Mark where platelets are.
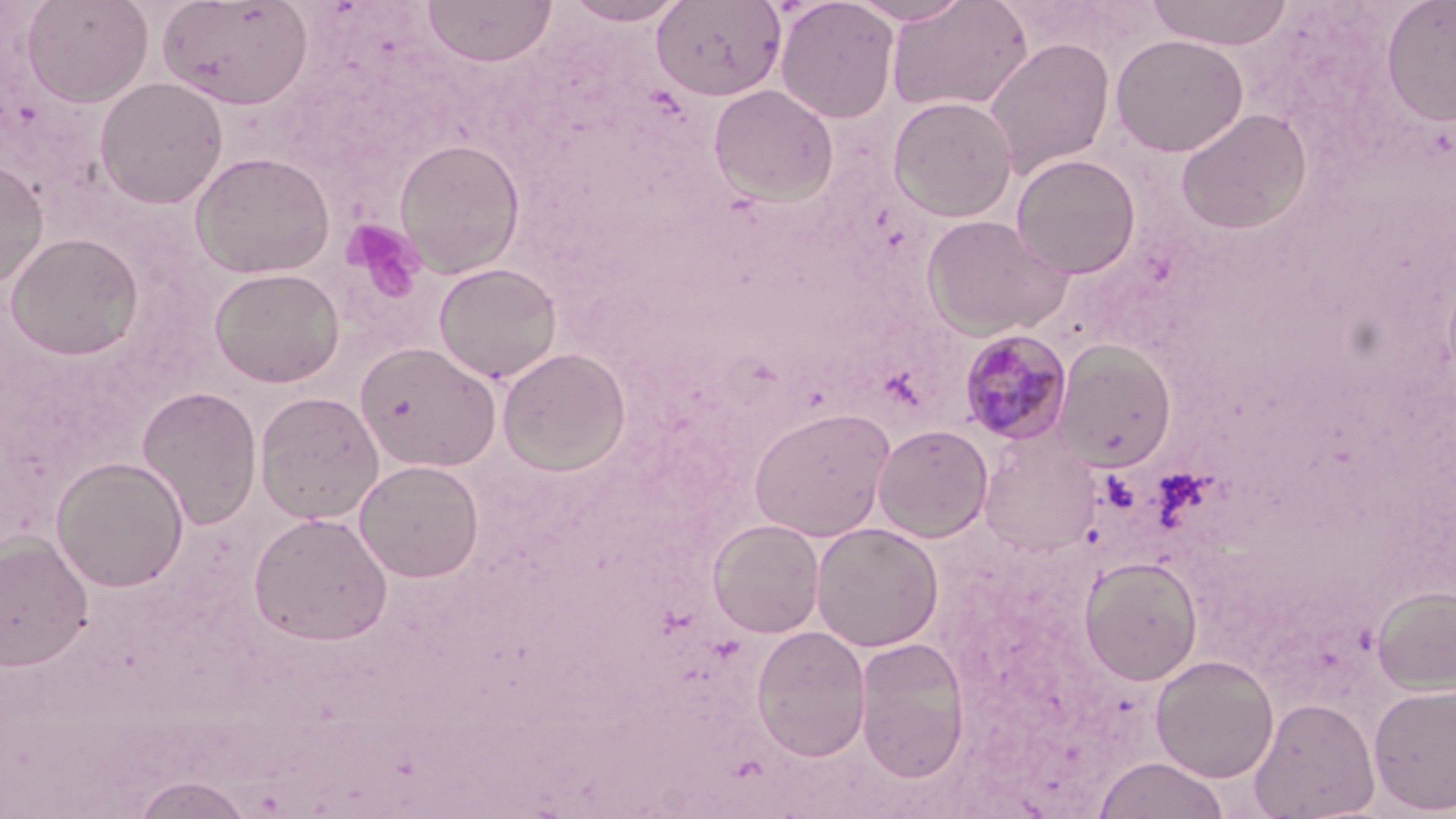
Approximate bounding boxes as (x1, y1, x2, y2) in pixels.
Platelets: (342, 218, 427, 306).

Plasmodium malariae-infected red blood cell locations: (958, 329, 1074, 445). Uninfected red blood cell locations: (22, 0, 153, 108), (422, 0, 557, 67), (651, 0, 787, 101), (775, 0, 899, 123), (847, 0, 974, 25), (886, 0, 1032, 114), (1143, 0, 1295, 49), (157, 1, 314, 111), (562, 1, 688, 26), (1380, 1, 1456, 126), (1110, 33, 1249, 156), (983, 37, 1115, 179), (94, 76, 229, 209), (708, 84, 839, 206), (888, 95, 1018, 221), (1175, 108, 1313, 235), (394, 138, 526, 278), (190, 151, 335, 279), (1010, 153, 1141, 279), (0, 158, 49, 292), (922, 213, 1072, 339), (5, 232, 145, 360), (432, 262, 563, 383), (208, 267, 345, 388), (1054, 341, 1177, 472), (355, 342, 502, 472), (498, 347, 631, 475), (136, 385, 262, 530), (254, 391, 385, 524), (749, 406, 896, 541), (873, 423, 993, 542), (977, 434, 1103, 559), (51, 456, 189, 592), (354, 460, 484, 581), (249, 512, 393, 645), (707, 519, 825, 638), (811, 522, 944, 652), (0, 534, 94, 670), (1080, 557, 1203, 685), (1372, 585, 1456, 694), (751, 625, 871, 762), (853, 637, 971, 781), (1151, 655, 1279, 783), (1368, 682, 1456, 815), (1249, 697, 1380, 818), (1093, 756, 1229, 819), (131, 775, 256, 818). Slide-level diagnosis: Plasmodium malariae. 1000x magnification. Optical microscopy. One field of a larger specimen. May-Grünwald-Giemsa-stained preparation. Image is 1456×819 pixels. Thin blood smear.